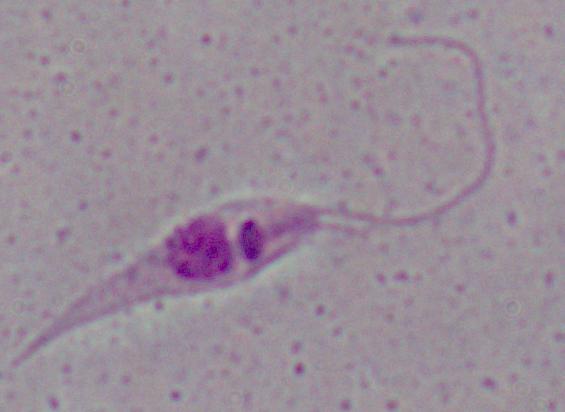
Micrograph. 1000x magnification. A Leishmania parasite is shown.